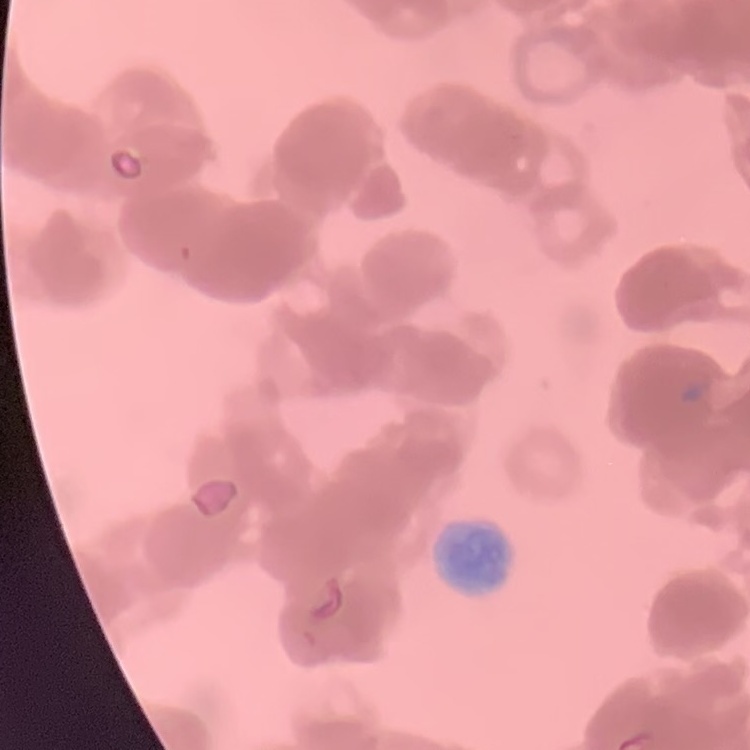
Summary:
  - Erythrocyte morphology: rouleaux formation
  - Image type: square crop of a larger photomicrograph
  - Preparation: thin blood film
  - Stain: Field's or Giemsa